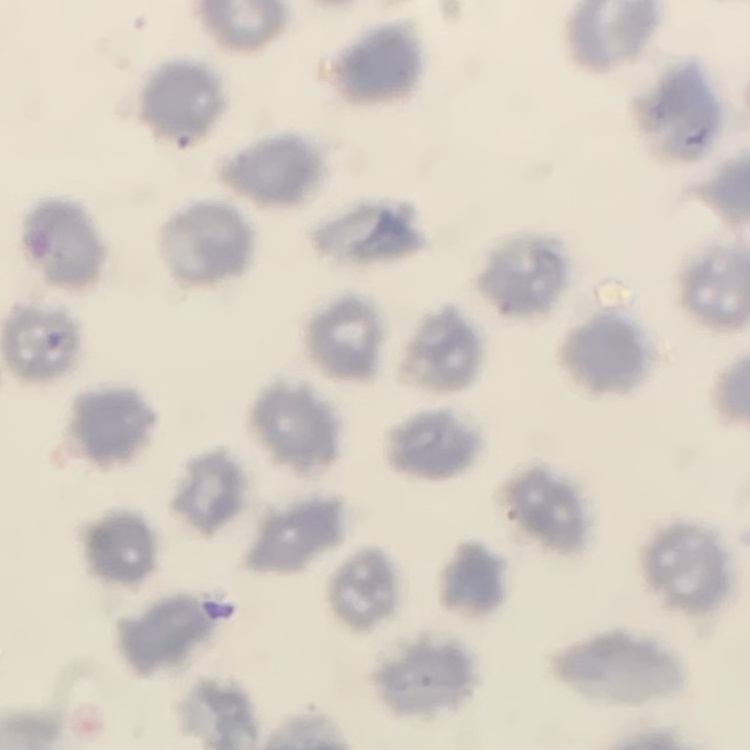

erythrocyte_morphology: no rouleaux formation
image_type: one tile cut from a larger photomicrograph
stain: Field's or Giemsa
preparation: thin blood film